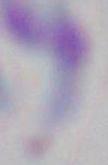
Summary:
  - Modality: micrograph
  - Magnification: 1000x
  - Identification: Toxoplasma gondii